Identify the parasite.
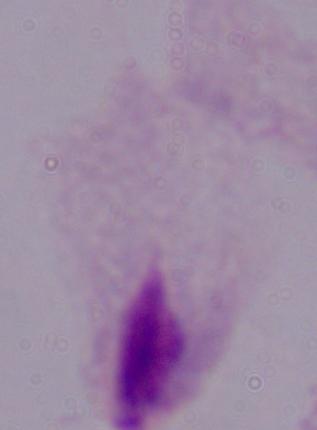

A trichomonad.

magnification: 1000x
modality: micrograph